State which parasite is depicted.
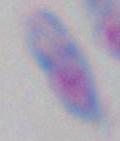

This is Toxoplasma gondii.

1000x magnification. Photomicrograph.